Locate platelets.
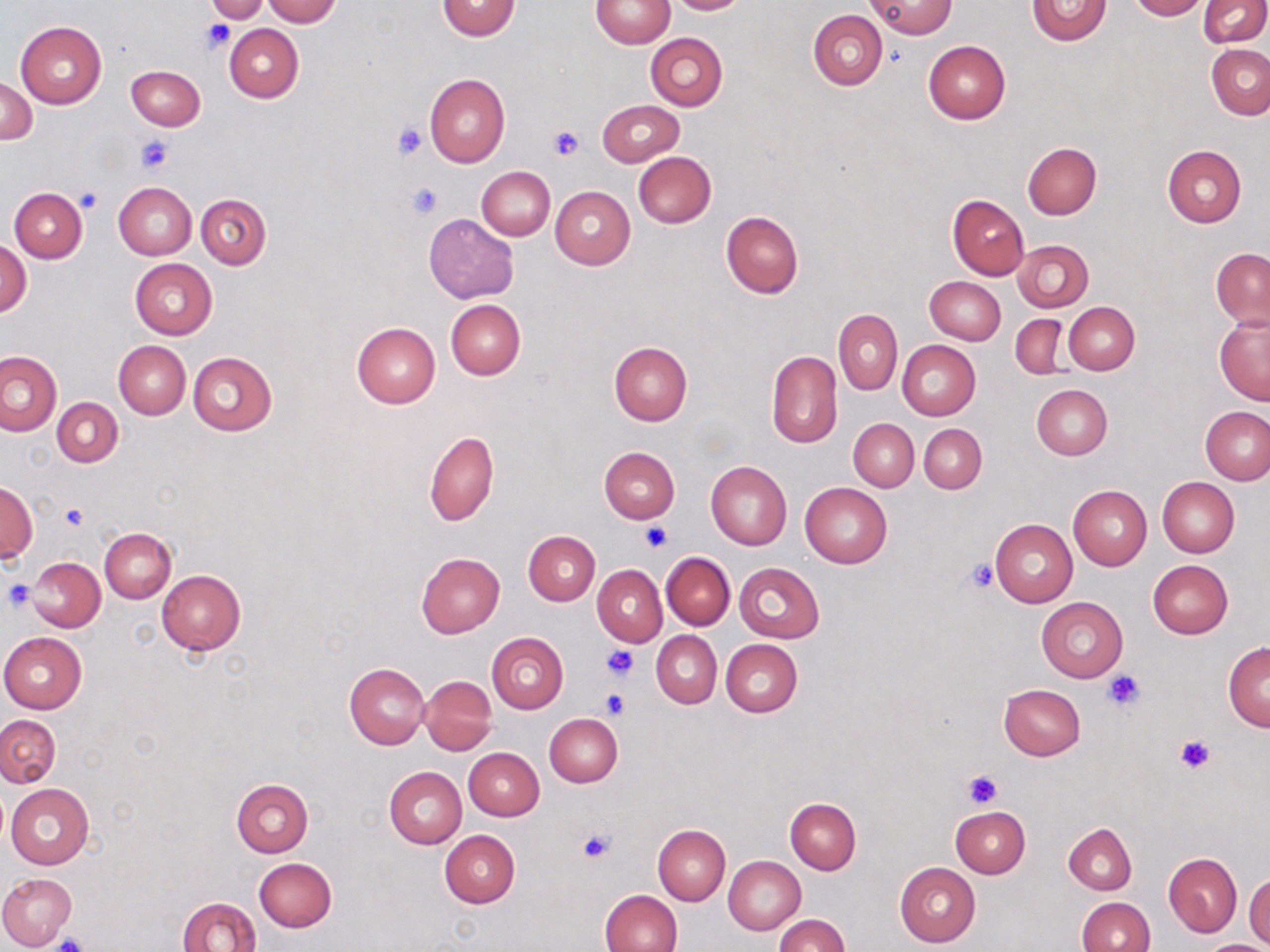

Approximate bounding boxes as named x1/y1/x2/y2 corners in pixels.
Platelets: (x1=202, y1=18, x2=234, y2=53), (x1=392, y1=121, x2=428, y2=160), (x1=548, y1=125, x2=585, y2=161), (x1=136, y1=136, x2=173, y2=172), (x1=406, y1=183, x2=443, y2=219), (x1=78, y1=189, x2=103, y2=212), (x1=60, y1=504, x2=88, y2=529), (x1=641, y1=521, x2=670, y2=551), (x1=964, y1=559, x2=999, y2=592), (x1=3, y1=580, x2=36, y2=611), (x1=601, y1=644, x2=638, y2=681), (x1=1103, y1=670, x2=1145, y2=711), (x1=600, y1=689, x2=630, y2=718), (x1=1175, y1=735, x2=1216, y2=773), (x1=962, y1=770, x2=1001, y2=807), (x1=577, y1=828, x2=617, y2=863), (x1=51, y1=934, x2=92, y2=952).

slide-level diagnosis = no evidence of blood parasites
field of view = one of a larger specimen
preparation = thin blood film
stain = May-Grünwald-Giemsa
uninfected red blood cell locations = approximate bounding boxes as named x1/y1/x2/y2 corners in pixels: (x1=263, y1=0, x2=341, y2=26), (x1=591, y1=0, x2=673, y2=49), (x1=665, y1=0, x2=748, y2=15), (x1=1026, y1=0, x2=1112, y2=45), (x1=1127, y1=0, x2=1207, y2=20), (x1=205, y1=1, x2=271, y2=23), (x1=437, y1=1, x2=521, y2=40), (x1=868, y1=1, x2=957, y2=38), (x1=1198, y1=1, x2=1269, y2=48), (x1=809, y1=11, x2=887, y2=90), (x1=15, y1=22, x2=106, y2=108), (x1=225, y1=23, x2=303, y2=102), (x1=646, y1=33, x2=727, y2=110), (x1=923, y1=40, x2=1011, y2=124), (x1=1206, y1=44, x2=1270, y2=119), (x1=126, y1=65, x2=205, y2=131), (x1=424, y1=74, x2=509, y2=167), (x1=1, y1=76, x2=36, y2=144), (x1=597, y1=100, x2=683, y2=166), (x1=1023, y1=143, x2=1101, y2=219), (x1=1162, y1=145, x2=1246, y2=227), (x1=632, y1=151, x2=716, y2=227), (x1=477, y1=166, x2=555, y2=240), (x1=114, y1=181, x2=195, y2=259), (x1=550, y1=186, x2=635, y2=269), (x1=10, y1=187, x2=87, y2=262), (x1=196, y1=193, x2=271, y2=268), (x1=947, y1=194, x2=1029, y2=280), (x1=720, y1=211, x2=804, y2=298), (x1=423, y1=212, x2=519, y2=304), (x1=1, y1=237, x2=31, y2=318), (x1=1013, y1=240, x2=1093, y2=312), (x1=1211, y1=247, x2=1270, y2=330), (x1=130, y1=258, x2=217, y2=339), (x1=924, y1=277, x2=1005, y2=345), (x1=446, y1=299, x2=526, y2=380), (x1=1064, y1=302, x2=1140, y2=374), (x1=834, y1=309, x2=902, y2=395), (x1=1213, y1=313, x2=1270, y2=407), (x1=1010, y1=314, x2=1067, y2=378), (x1=352, y1=322, x2=441, y2=408), (x1=114, y1=340, x2=191, y2=419), (x1=898, y1=340, x2=981, y2=419), (x1=609, y1=341, x2=693, y2=424), (x1=0, y1=351, x2=62, y2=436), (x1=766, y1=351, x2=842, y2=447), (x1=188, y1=352, x2=278, y2=436), (x1=1031, y1=383, x2=1113, y2=460), (x1=53, y1=398, x2=122, y2=467), (x1=1201, y1=408, x2=1269, y2=484), (x1=849, y1=419, x2=918, y2=491), (x1=918, y1=423, x2=986, y2=493), (x1=425, y1=431, x2=499, y2=525), (x1=599, y1=447, x2=680, y2=523), (x1=706, y1=462, x2=792, y2=549), (x1=1157, y1=476, x2=1240, y2=557), (x1=1, y1=482, x2=37, y2=562), (x1=800, y1=482, x2=891, y2=568), (x1=1068, y1=486, x2=1151, y2=570), (x1=991, y1=520, x2=1078, y2=606), (x1=100, y1=528, x2=175, y2=602), (x1=523, y1=530, x2=599, y2=605), (x1=415, y1=553, x2=505, y2=638), (x1=662, y1=553, x2=734, y2=629), (x1=28, y1=557, x2=105, y2=631), (x1=1148, y1=560, x2=1232, y2=639), (x1=735, y1=562, x2=824, y2=642), (x1=593, y1=565, x2=667, y2=646), (x1=157, y1=570, x2=246, y2=655), (x1=1037, y1=596, x2=1128, y2=682), (x1=652, y1=631, x2=721, y2=708), (x1=1, y1=632, x2=86, y2=713), (x1=488, y1=632, x2=568, y2=713), (x1=721, y1=639, x2=802, y2=718), (x1=1224, y1=642, x2=1270, y2=731), (x1=344, y1=662, x2=429, y2=748), (x1=420, y1=675, x2=497, y2=755), (x1=998, y1=684, x2=1086, y2=760), (x1=545, y1=714, x2=622, y2=786), (x1=0, y1=715, x2=60, y2=787), (x1=463, y1=748, x2=544, y2=820), (x1=384, y1=766, x2=467, y2=849), (x1=232, y1=779, x2=313, y2=857), (x1=5, y1=783, x2=94, y2=868), (x1=785, y1=798, x2=861, y2=874), (x1=950, y1=805, x2=1030, y2=877), (x1=1064, y1=823, x2=1136, y2=894), (x1=653, y1=824, x2=731, y2=905), (x1=440, y1=830, x2=520, y2=908), (x1=1164, y1=853, x2=1241, y2=936), (x1=724, y1=855, x2=806, y2=935), (x1=254, y1=857, x2=336, y2=932), (x1=894, y1=862, x2=981, y2=947), (x1=0, y1=872, x2=76, y2=949), (x1=1244, y1=873, x2=1270, y2=946), (x1=599, y1=890, x2=682, y2=952), (x1=178, y1=897, x2=260, y2=952), (x1=1077, y1=897, x2=1154, y2=952), (x1=775, y1=914, x2=849, y2=952), (x1=1201, y1=941, x2=1267, y2=951)
magnification = 1000x
modality = light microscopy
image size = 1270×952 pixels